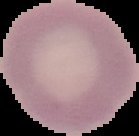
{
  "preparation": "thin blood film",
  "image_size": "139×136 pixels",
  "image_type": "cell region segmented out of the field of view; surrounding area masked to black",
  "malaria_status": "uninfected"
}